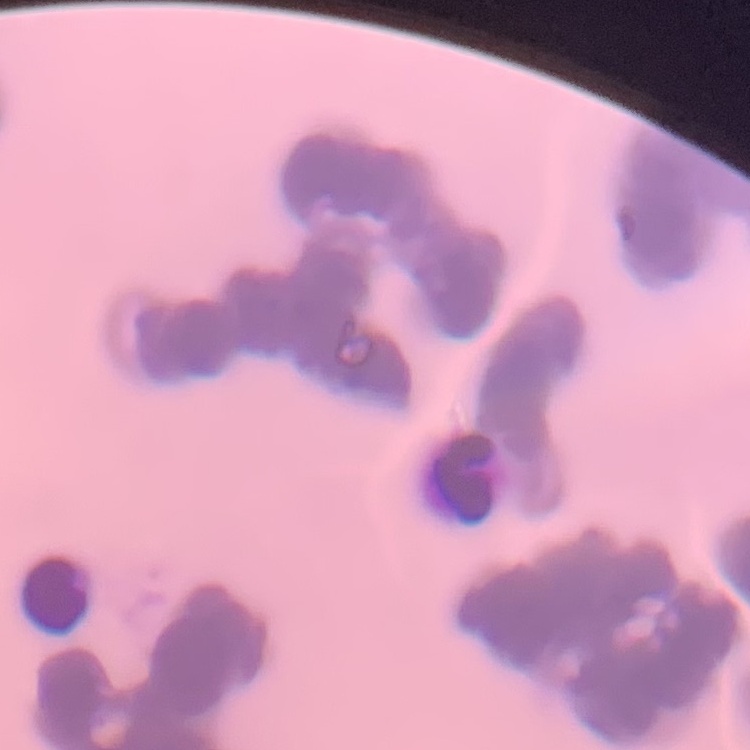

Summary:
  - Erythrocyte morphology: rouleaux formation
  - Stain: Field's or Giemsa
  - Preparation: thin blood film
  - Image type: square crop of a larger photomicrograph